Report the malaria status of this cell.
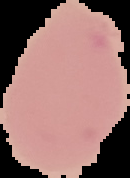

It is uninfected.

From a thin blood smear. Segmented cell region on a black background. Image is 130×178 pixels.